Locate every Plasmodium parasite.
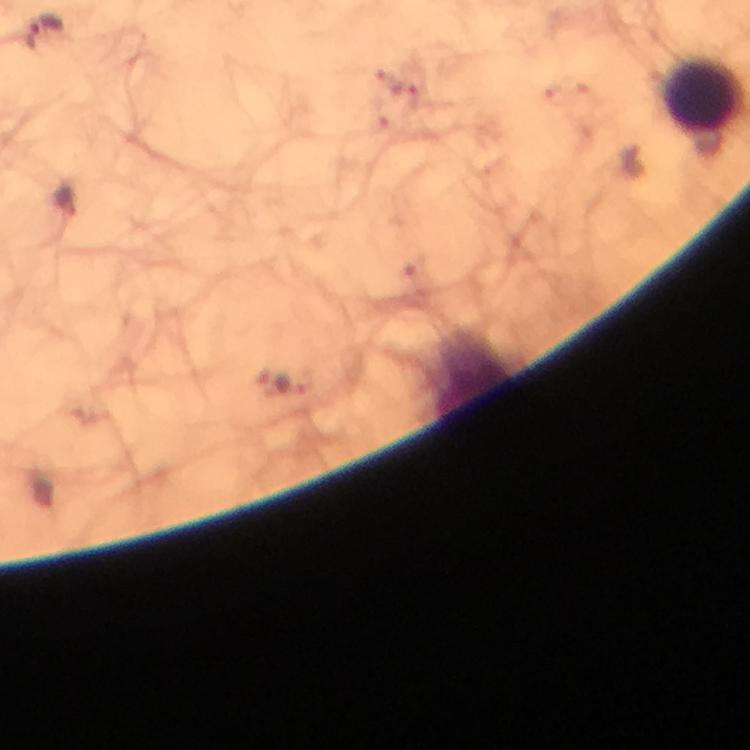
Approximate centers as [x, y] in pixels.
Plasmodium parasites: [46, 34], [67, 199], [285, 384].

100x magnification. Smartphone photograph taken through a microscope. Cropped region of a single field of view. Immersion oil was used. Thick smear. From a malaria diagnostic workup. Giemsa stain. Image is 750×750 pixels.